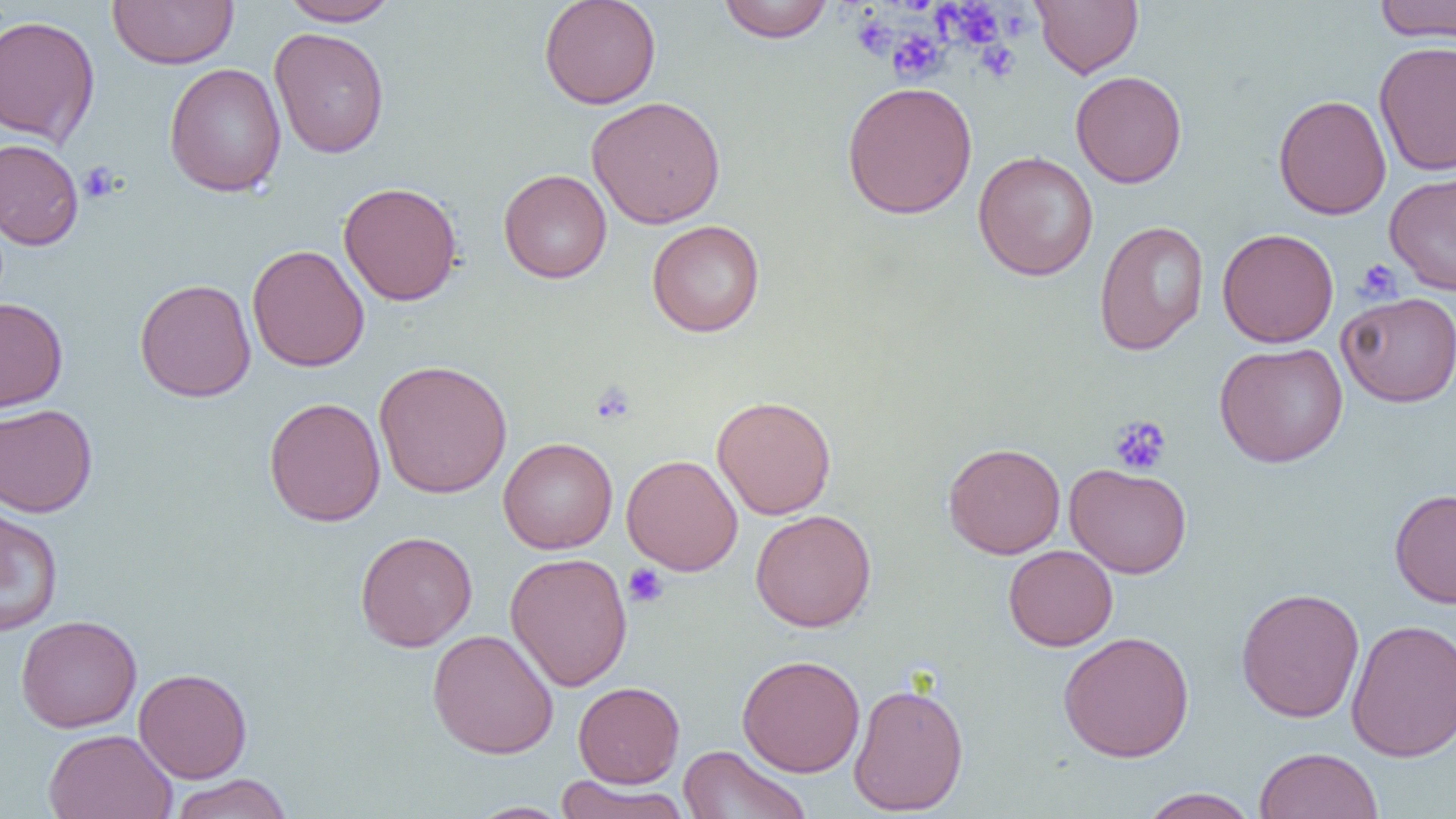

Approximate bounding boxes as [x1, y1, x2, y2] in pixels. Platelet locations: [937, 2, 1005, 50], [1007, 6, 1035, 39], [852, 15, 896, 59], [887, 30, 947, 83], [976, 41, 1020, 82], [79, 161, 120, 204], [1355, 259, 1403, 303], [590, 383, 636, 425], [1108, 415, 1172, 476], [623, 563, 669, 608]. Uninfected red blood cell locations: [107, 0, 238, 69], [539, 0, 662, 109], [1032, 0, 1143, 78], [1373, 0, 1456, 43], [279, 1, 401, 26], [716, 1, 836, 43], [0, 13, 101, 147], [269, 27, 390, 158], [1373, 40, 1456, 177], [163, 63, 286, 197], [1070, 70, 1187, 188], [841, 81, 978, 219], [1273, 94, 1391, 219], [587, 95, 727, 229], [0, 138, 84, 250], [973, 150, 1099, 281], [498, 169, 612, 283], [1384, 170, 1456, 295], [338, 182, 463, 306], [647, 220, 766, 337], [1093, 220, 1209, 356], [1217, 228, 1338, 348], [247, 244, 370, 372], [134, 278, 257, 402], [1337, 292, 1456, 407], [0, 297, 68, 412], [1214, 341, 1348, 468], [373, 359, 513, 499], [711, 395, 837, 520], [263, 397, 387, 526], [0, 403, 98, 517], [498, 437, 618, 554], [942, 442, 1066, 559], [621, 454, 743, 575], [1065, 462, 1192, 578], [1389, 488, 1456, 608], [0, 507, 64, 637], [750, 510, 877, 632], [355, 531, 477, 652], [1003, 545, 1118, 651], [505, 552, 632, 691], [1235, 587, 1365, 723], [15, 614, 142, 733], [1345, 618, 1456, 762], [427, 629, 559, 759], [1058, 631, 1194, 762], [737, 654, 866, 778], [133, 668, 253, 783], [573, 681, 685, 787], [848, 681, 969, 816], [43, 728, 178, 819], [678, 744, 811, 819], [1254, 746, 1383, 819], [169, 773, 293, 819], [553, 775, 691, 819], [1137, 788, 1260, 818], [466, 801, 574, 819]. Slide-level diagnosis: negative for blood parasites. Optical microscopy. Thin blood film. Single field of view. Image is 1456×819 pixels. 1000x magnification.